Locate every blood parasite and identify its species.
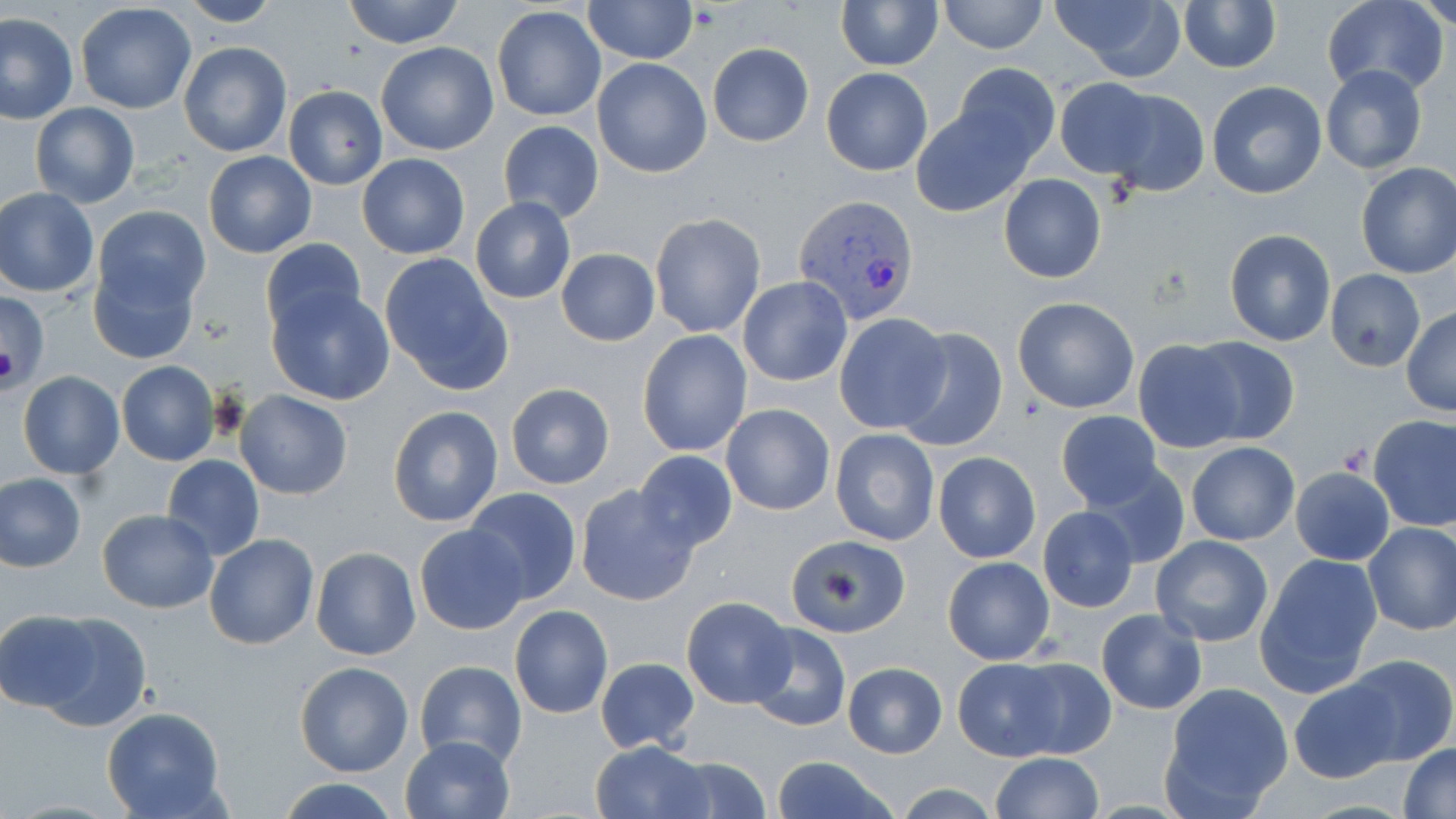
Approximate bounding boxes as (x1,y1)-(x2,y2) corner pairs in pixels.
Plasmodium vivax-infected red blood cells: (794,195)-(917,323).
No Plasmodium falciparum, Plasmodium ovale, Plasmodium malariae, Babesia divergens, or Trypanosoma brucei observed.

slide-level diagnosis = Plasmodium vivax
field of view = single
preparation = thin blood smear
image size = 1456×819 pixels
uninfected red blood cell locations = approximate bounding boxes as (x1,y1)-(x2,y2) corner pairs in pixels: (172,0)-(282,27), (343,0)-(465,48), (938,0)-(1049,54), (1324,0)-(1450,98), (1417,0)-(1456,31), (584,1)-(698,64), (834,1)-(943,70), (1047,1)-(1186,81), (1177,2)-(1282,73), (75,3)-(197,114), (493,5)-(606,123), (1,12)-(77,124), (179,40)-(292,158), (376,40)-(498,156), (706,42)-(814,147), (592,57)-(712,178), (950,63)-(1060,171), (821,66)-(933,177), (1320,66)-(1428,176), (1055,77)-(1161,179), (1207,82)-(1328,199), (283,85)-(387,189), (1102,90)-(1209,197), (30,102)-(140,208), (910,102)-(1039,217), (497,120)-(603,224), (203,151)-(316,258), (356,155)-(470,258), (1354,161)-(1456,278), (1000,174)-(1107,284), (0,188)-(99,298), (471,197)-(576,304), (93,205)-(210,312), (650,211)-(766,338), (1224,229)-(1336,347), (259,237)-(367,337), (555,247)-(661,346), (377,253)-(515,396), (88,257)-(199,366), (1324,269)-(1427,371), (737,276)-(852,387), (266,284)-(396,406), (1,291)-(51,387), (688,293)-(843,418), (1013,296)-(1139,414), (1402,306)-(1456,416), (835,312)-(952,433), (895,327)-(1008,454), (637,329)-(752,458), (1185,336)-(1300,448), (1131,338)-(1246,454), (116,361)-(220,466), (17,370)-(124,479), (505,382)-(616,489), (235,390)-(353,499), (720,402)-(835,516), (387,406)-(504,527), (1055,410)-(1164,509), (1368,414)-(1456,531), (830,427)-(939,545), (1186,441)-(1300,546), (632,450)-(739,554), (934,452)-(1039,563), (162,454)-(265,561), (1084,462)-(1191,570), (1290,466)-(1396,565), (0,473)-(86,571), (575,484)-(700,606), (463,488)-(583,605), (1038,506)-(1140,612), (96,507)-(219,613), (1362,521)-(1456,635), (414,523)-(530,635), (205,534)-(320,651), (786,534)-(909,639), (1151,535)-(1273,647), (312,547)-(421,660), (1254,553)-(1383,699), (942,557)-(1055,665), (681,597)-(794,708), (510,605)-(613,718), (28,609)-(151,731), (0,610)-(104,712), (1096,610)-(1207,714), (746,622)-(851,732), (1338,653)-(1456,768), (596,655)-(700,754), (951,656)-(1066,759), (1001,657)-(1115,758), (413,660)-(527,766), (295,661)-(415,777), (841,662)-(947,758), (1288,677)-(1403,783), (1160,683)-(1293,816), (103,708)-(228,818), (400,735)-(514,818), (590,740)-(713,819), (1399,742)-(1456,818), (991,752)-(1103,819), (662,755)-(775,819), (769,757)-(902,819), (277,777)-(402,819)
platelet locations = approximate bounding boxes as (x1,y1)-(x2,y2) corner pairs in pixels: (1336,442)-(1369,477)
stain = May-Grünwald-Giemsa
modality = light microscopy
magnification = 1000x